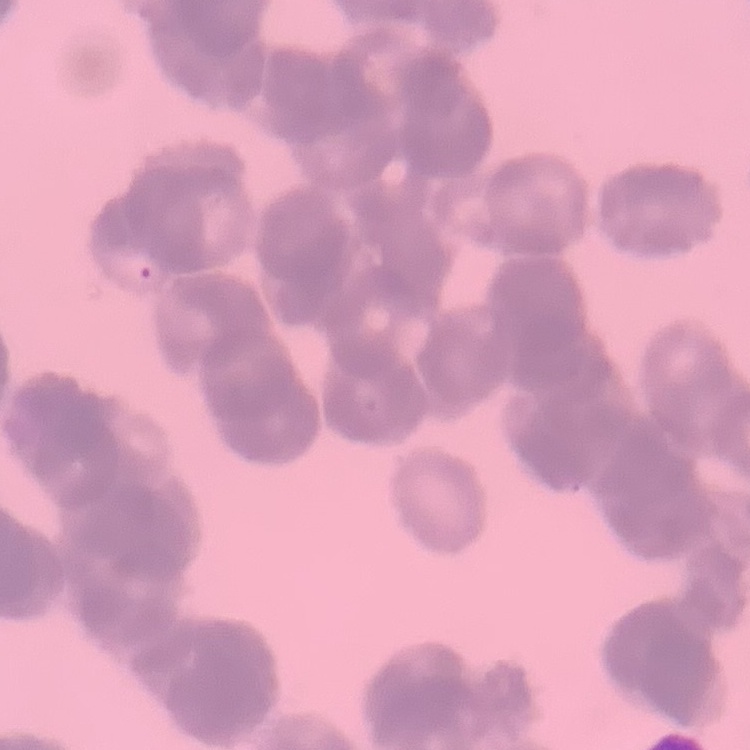
Summary:
  - Erythrocyte morphology: rouleaux formation
  - Image type: square crop of a larger photomicrograph
  - Stain: Field's or Giemsa
  - Preparation: thin blood film